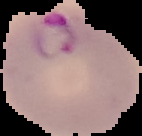

Summary:
  - Image type: cell region segmented out of the field of view; surrounding area masked to black
  - Preparation: thin blood film
  - Image size: 142×136 pixels
  - Malaria status: parasitized